Look for Plasmodium parasites.
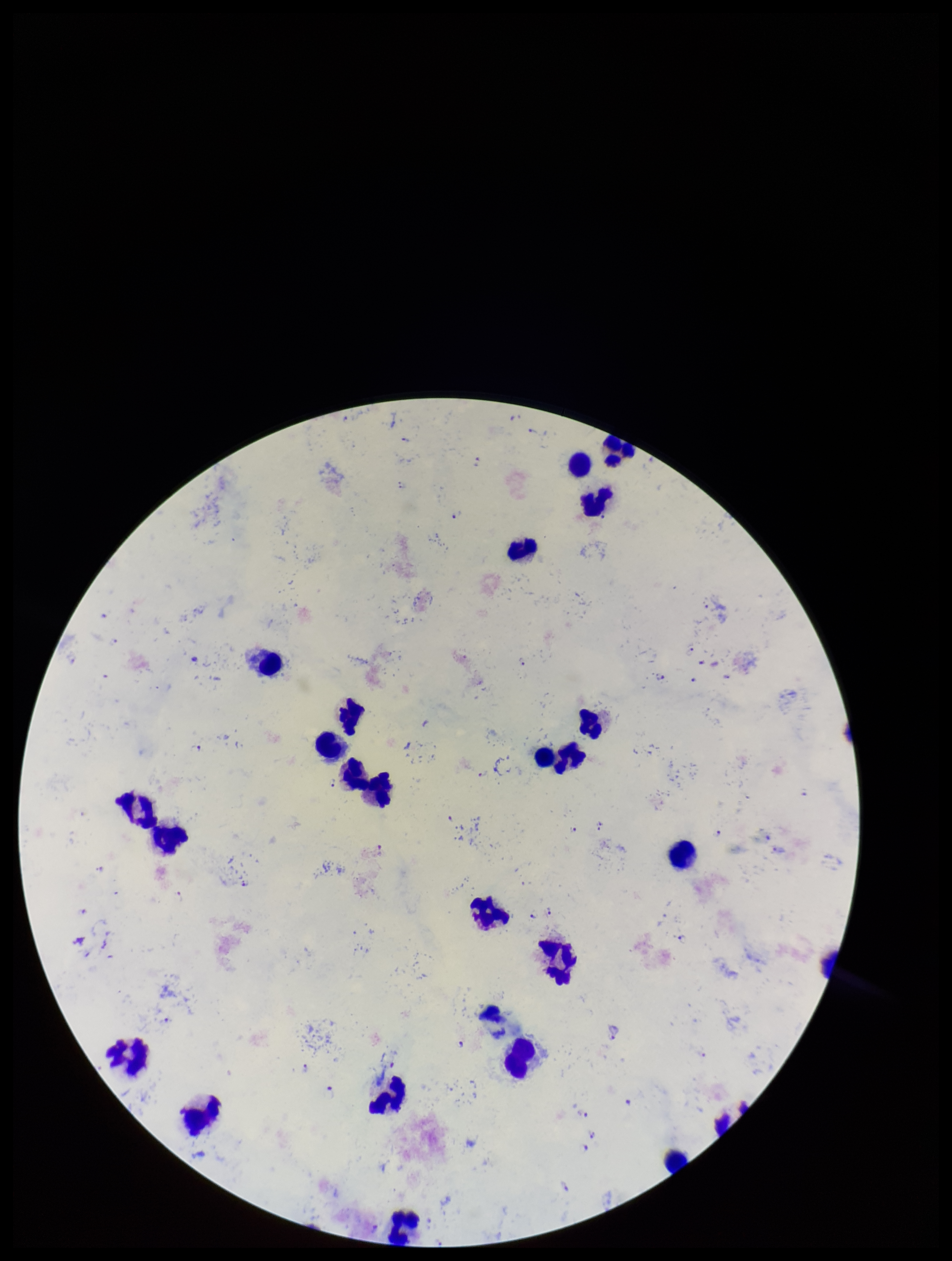
Identified.

{
  "field_of_view": "one from this slide",
  "capture": "smartphone photograph through the microscope eyepiece",
  "patient_malaria_status": "infected",
  "preparation": "thick blood smear",
  "stain": "Giemsa",
  "image_size": "952×1261 pixels",
  "parasite_count": 33,
  "species_reported_for_this_patient": "Plasmodium falciparum",
  "leukocyte_count": 23
}